Classify this cell by malaria status.
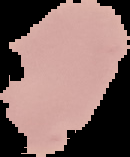

Uninfected.

Summary:
  - Image size: 130×157 pixels
  - Image type: segmented cell region on a black background
  - Preparation: thin blood film